Point out each Plasmodium parasite and each leukocyte.
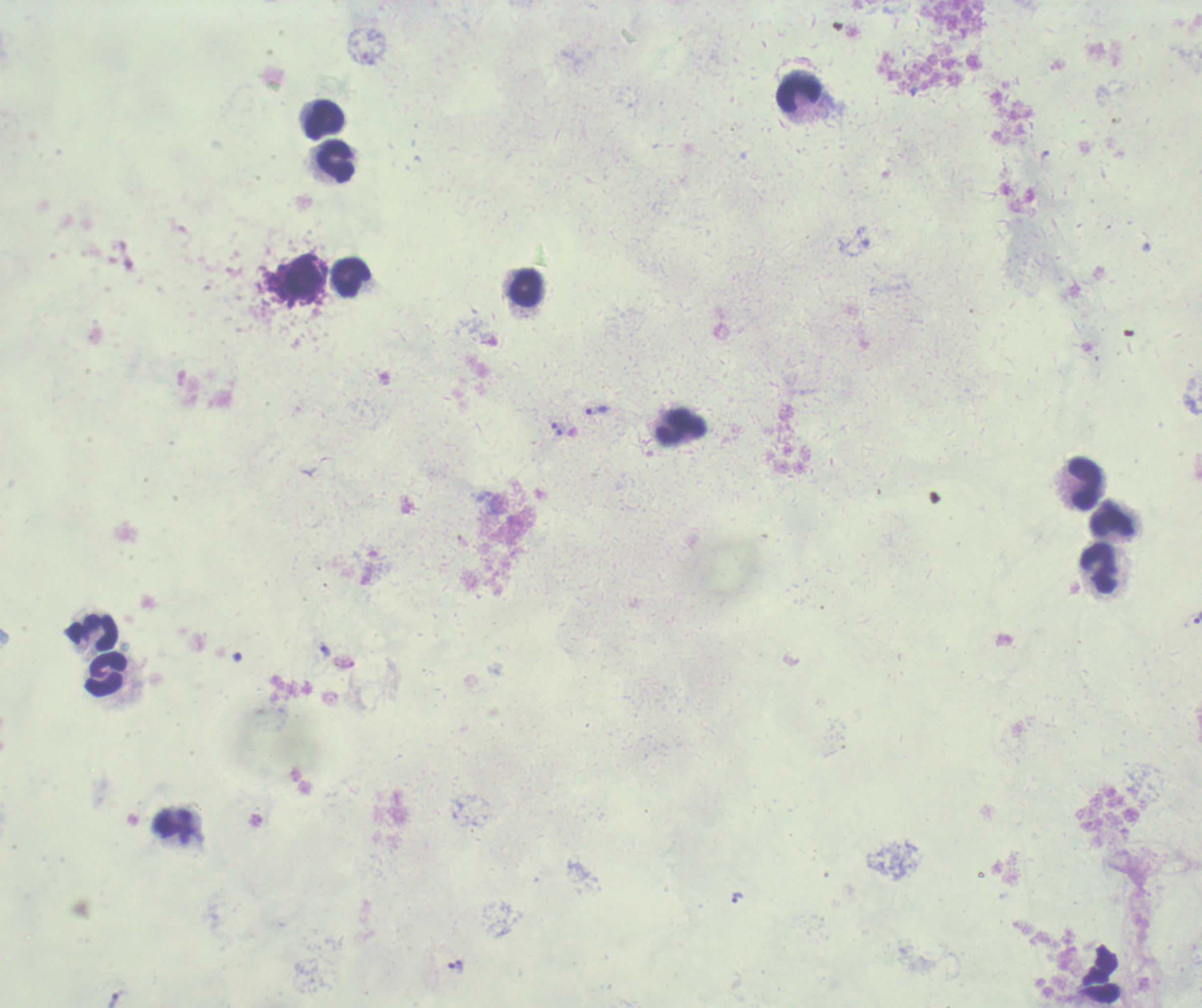
Approximate object centers, in pixels from the top-left corner.
Trophozoites: (x=596, y=410), (x=1197, y=617), (x=325, y=652), (x=735, y=898), (x=456, y=967).
No schizont or gametocyte forms observed.
Leukocytes: (x=798, y=92), (x=324, y=121), (x=335, y=162), (x=349, y=277), (x=526, y=290), (x=680, y=427), (x=1083, y=482), (x=1111, y=521), (x=1099, y=569), (x=92, y=630), (x=106, y=675), (x=173, y=826).

image_size: 1202×1008 pixels
field_of_view: single
stain: Romanowsky
preparation: thick smear of blood
magnification: 100x
background_quality: unsatisfactory
context: previously used in a real diagnosis